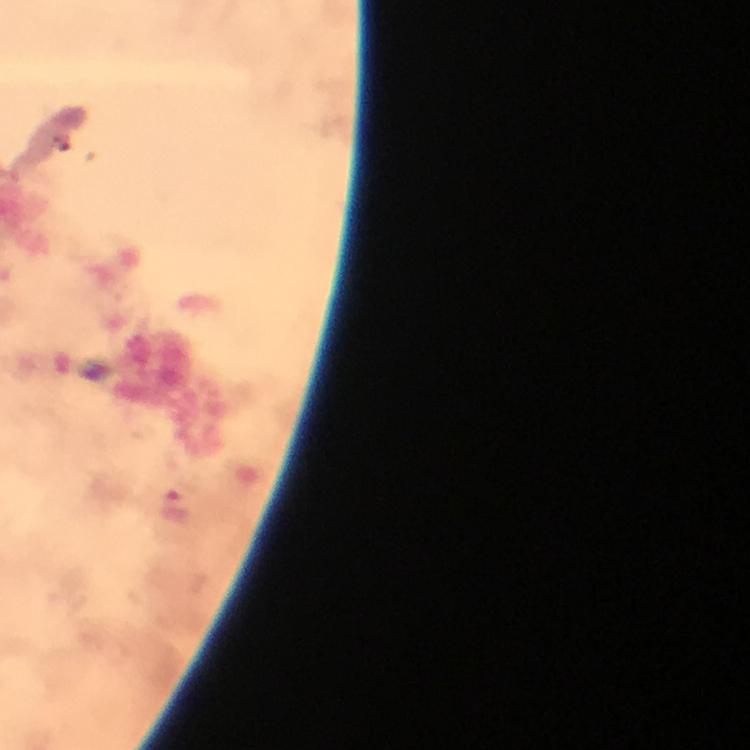

malaria_parasite_locations: 'approximate centers as [x, y] in pixels: [178, 513]'
context: from a diagnostic examination for malaria
capture: smartphone photograph through a microscope
immersion_oil: applied
stain: Giemsa
image_size: 750×750 pixels
cropped_from: one field of view
preparation: thick smear
magnification: 100x